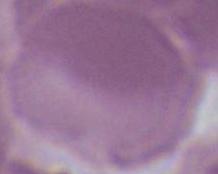

{
  "modality": "micrograph",
  "identification": "red blood cell",
  "magnification": "1000x"
}